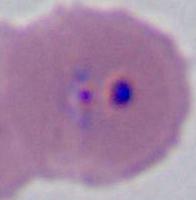
Summary:
  - Identification: Plasmodium
  - Magnification: 400x or 1000x
  - Modality: photomicrograph